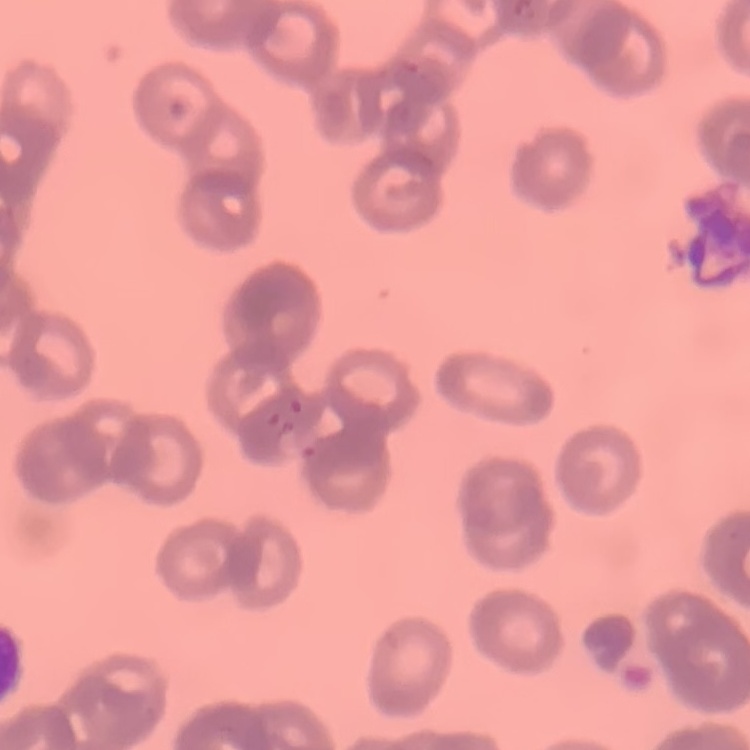
erythrocyte morphology = rouleaux formation
stain = Field's or Giemsa
preparation = thin blood smear
image type = one tile cut from a larger photomicrograph